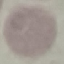

malaria status = uninfected
stain = Giemsa
image type = cell patch, automatically extracted from a larger field of view and resized to 64 × 64 pixels
preparation = thin blood smear
capture = smartphone camera at the microscope eyepiece